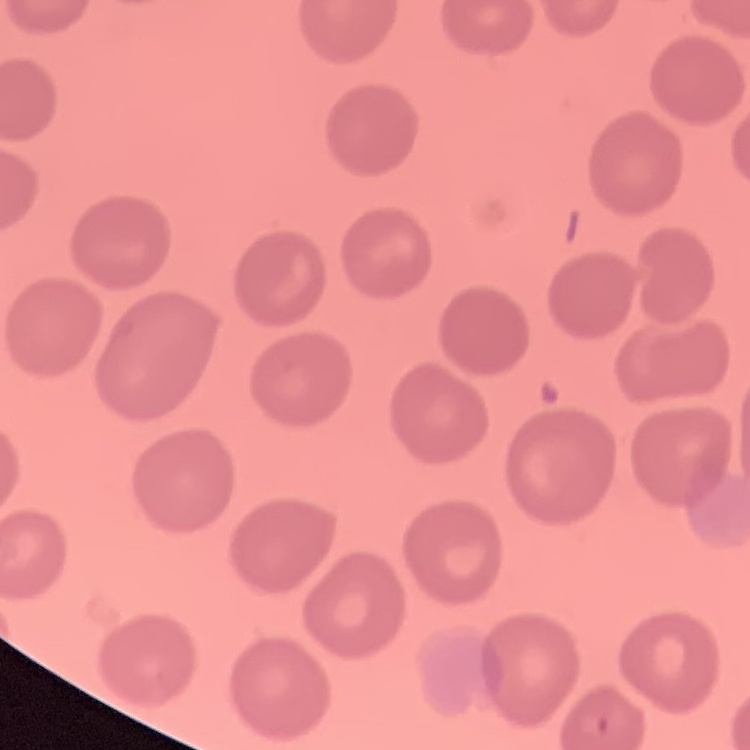

Summary:
  - Red blood cell morphology: no rouleaux formation
  - Preparation: thin blood film
  - Image type: square crop of a larger photomicrograph
  - Stain: Field's or Giemsa